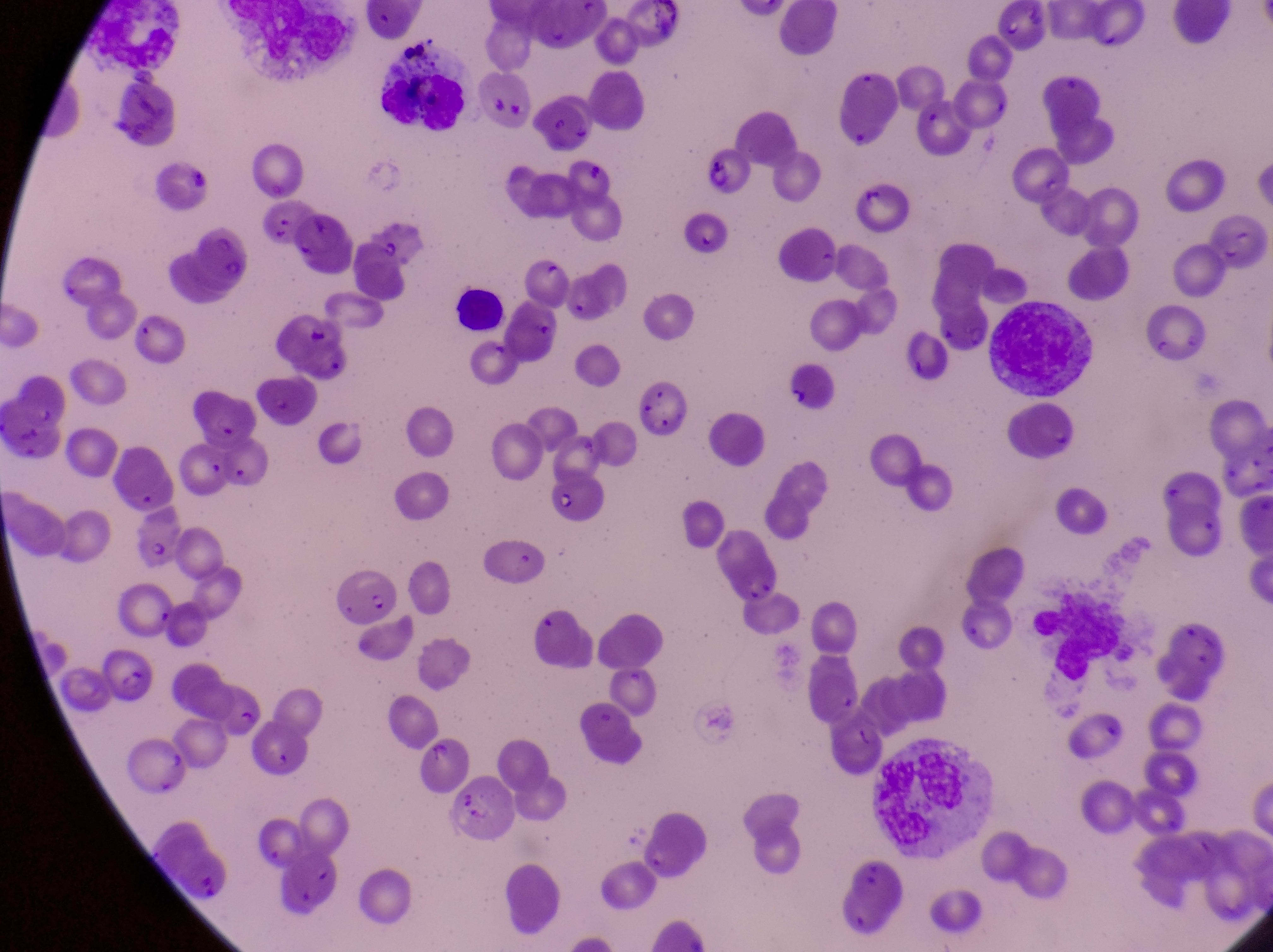

parasitised red blood cell locations = approximate bounding boxes as (left, top, right, bottom) in pixels: (701, 147, 756, 199), (861, 182, 913, 235), (679, 213, 729, 263), (187, 223, 252, 288), (785, 369, 840, 416), (632, 379, 687, 437), (199, 394, 256, 446), (549, 470, 619, 528), (127, 504, 187, 569), (720, 532, 787, 603), (327, 572, 394, 625), (97, 646, 160, 708), (251, 725, 311, 778), (421, 735, 473, 792)
leukocyte locations = approximate bounding boxes as (left, top, right, bottom) in pixels: (381, 63, 468, 132), (444, 278, 513, 338), (986, 299, 1098, 401), (1028, 586, 1127, 680), (874, 747, 981, 849)
country = Uganda
field of view = single
capture = smartphone photograph through the eyepiece of an Olympus CX-23 microscope
image size = 1273×952 pixels
artifact (platelet-like body, stain precipitate, or debris) locations = approximate bounding boxes as (left, top, right, bottom) in pixels: (397, 30, 439, 67), (541, 264, 566, 289), (484, 339, 521, 379)
preparation = thin blood smear
magnification = 1000x